Locate every malaria parasite.
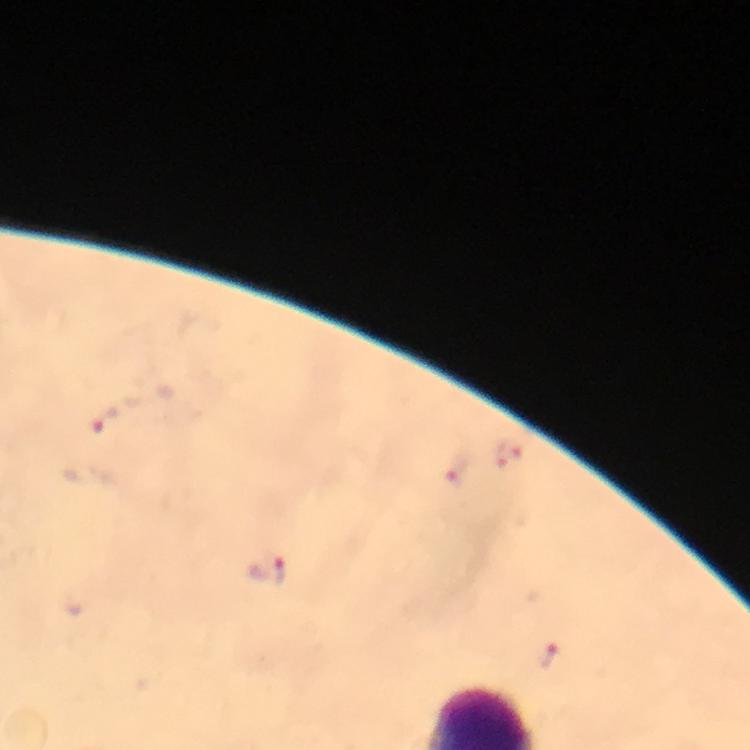
Approximate centers as [x, y] in pixels.
Malaria parasites: [508, 456], [455, 472], [268, 569], [546, 658].

{
  "stain": "Giemsa",
  "cropped_from": "one field of view",
  "preparation": "thick smear",
  "image_size": "750×750 pixels",
  "capture": "smartphone mounted on the microscope",
  "context": "from a diagnostic examination for malaria",
  "immersion_oil": "used",
  "magnification": "100x"
}